Report the malaria status of this cell.
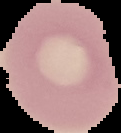
Uninfected.

Image is 121×133 pixels. Segmented cell region on a black background. From a thin blood smear.